Name the cell type shown.
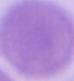
An erythrocyte.

1000x magnification. Photomicrograph.